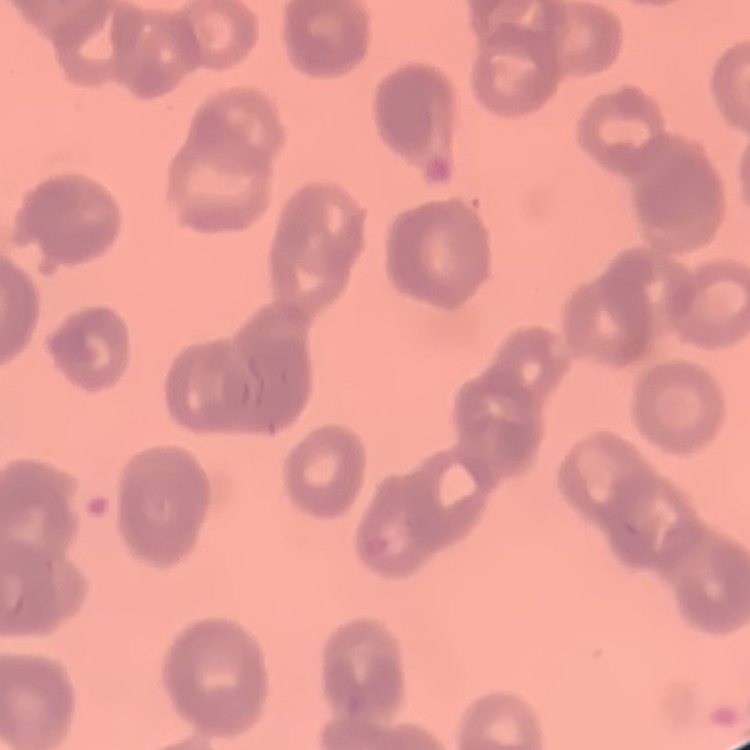

The red blood cells show rouleaux formation. Field's or Giemsa stain. Thin peripheral smear. One tile cut from a larger photomicrograph.